Locate every blood parasite and identify its species.
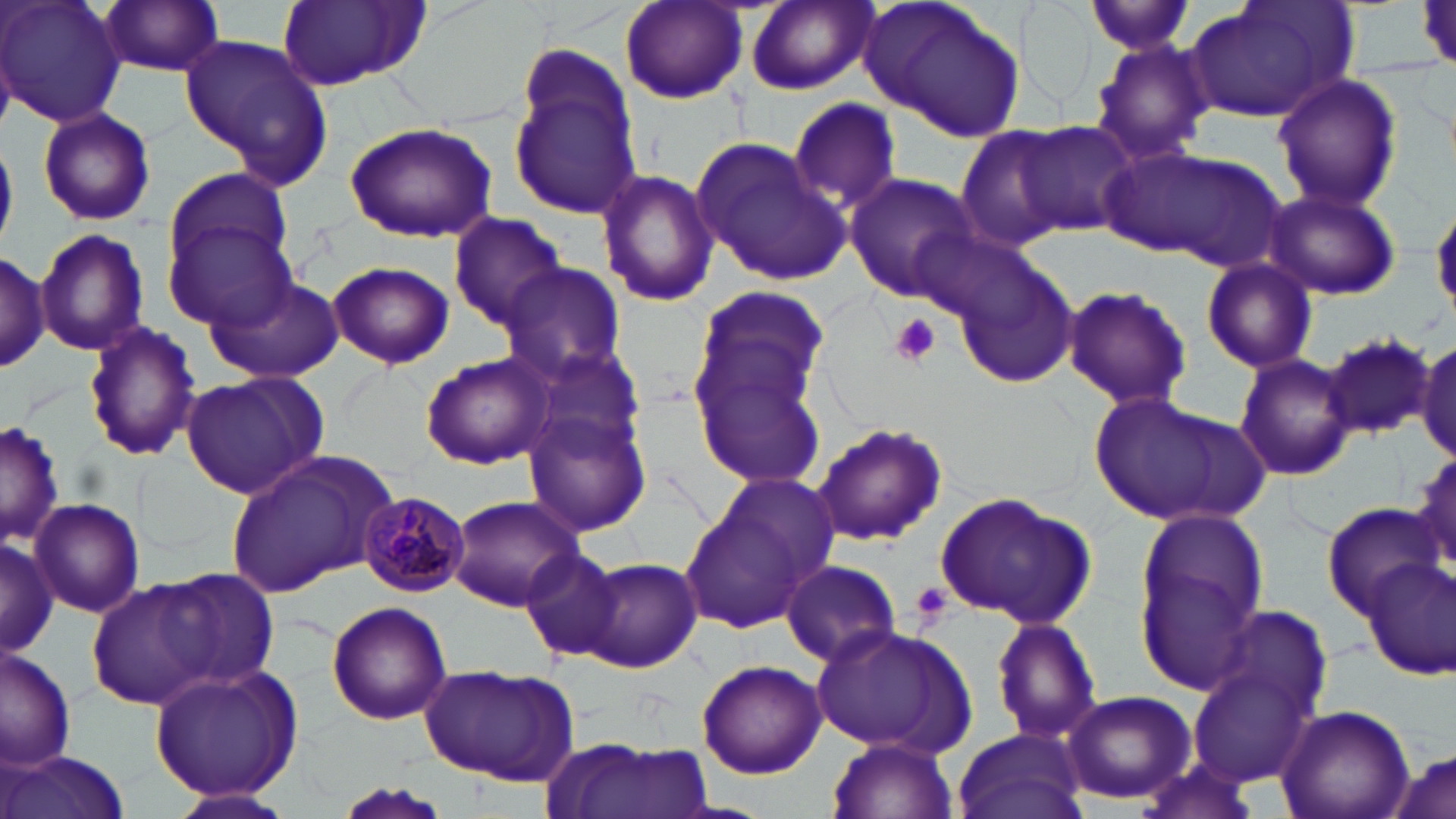
Approximate bounding boxes as (x1, y1, x2, y2) in pixels.
Plasmodium malariae-infected red blood cells: (357, 491, 470, 597).
No Plasmodium falciparum, Plasmodium ovale, Plasmodium vivax, Babesia divergens, or Trypanosoma brucei observed.

slide-level diagnosis = Plasmodium malariae
uninfected red blood cell locations = approximate bounding boxes as (x1, y1, x2, y2) in pixels: (1, 0, 125, 128), (98, 0, 227, 77), (276, 0, 429, 91), (618, 0, 750, 105), (745, 0, 876, 93), (864, 0, 1025, 143), (1016, 0, 1103, 116), (1185, 0, 1354, 124), (1082, 2, 1200, 57), (179, 32, 334, 185), (1087, 37, 1215, 167), (508, 46, 646, 224), (1270, 73, 1403, 212), (788, 96, 903, 211), (37, 106, 156, 227), (343, 121, 496, 243), (1015, 122, 1141, 235), (955, 126, 1074, 250), (692, 136, 852, 286), (1113, 145, 1288, 269), (594, 168, 720, 307), (161, 169, 298, 322), (842, 173, 981, 304), (1264, 185, 1401, 302), (1432, 200, 1456, 316), (448, 211, 569, 332), (34, 227, 149, 358), (0, 248, 50, 377), (947, 252, 1080, 390), (1200, 258, 1319, 374), (327, 260, 455, 369), (498, 261, 627, 384), (204, 273, 343, 383), (1060, 283, 1193, 410), (689, 284, 834, 423), (81, 321, 202, 461), (1320, 331, 1437, 440), (1415, 335, 1456, 464), (518, 340, 650, 463), (689, 347, 833, 490), (420, 352, 556, 469), (1234, 355, 1357, 480), (179, 372, 330, 502), (1087, 390, 1264, 525), (524, 405, 654, 534), (0, 420, 64, 548), (811, 420, 948, 546), (1408, 446, 1455, 580), (225, 450, 396, 598), (703, 469, 845, 602), (934, 491, 1095, 627), (447, 494, 587, 611), (29, 498, 144, 617), (680, 499, 809, 631), (1322, 504, 1442, 612), (1132, 508, 1270, 692), (0, 536, 57, 657), (519, 546, 624, 663), (1363, 554, 1456, 680), (581, 557, 702, 674), (780, 559, 900, 669), (124, 565, 284, 697), (88, 580, 219, 710), (326, 602, 452, 725), (1203, 604, 1336, 726), (989, 616, 1102, 747), (813, 624, 972, 753), (0, 646, 77, 772), (696, 658, 826, 777), (425, 664, 578, 787), (148, 665, 302, 800), (1187, 665, 1319, 789), (1060, 690, 1195, 805), (1273, 703, 1414, 819), (952, 726, 1090, 819), (550, 737, 709, 819), (828, 737, 957, 819), (1385, 743, 1456, 819), (3, 750, 129, 819), (1131, 754, 1263, 819), (325, 782, 455, 818), (163, 785, 298, 819)
preparation = thin blood film
modality = light microscopy
image size = 1456×819 pixels
magnification = 1000x
field of view = one of a larger specimen
stain = May-Grünwald-Giemsa
platelet locations = approximate bounding boxes as (x1, y1, x2, y2) in pixels: (889, 314, 942, 367), (910, 580, 953, 627)